Report the malaria status of this cell.
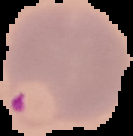

Parasitized.

image_size: 133×136 pixels
image_type: segmented cell region on a black background
preparation: thin blood film